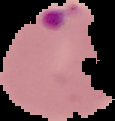
From a thin blood smear. Segmented cell region on a black background. Malaria status: parasitized. Image is 115×121 pixels.